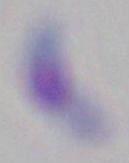

Captured at 1000x magnification. Photomicrograph. Toxoplasma gondii is shown.